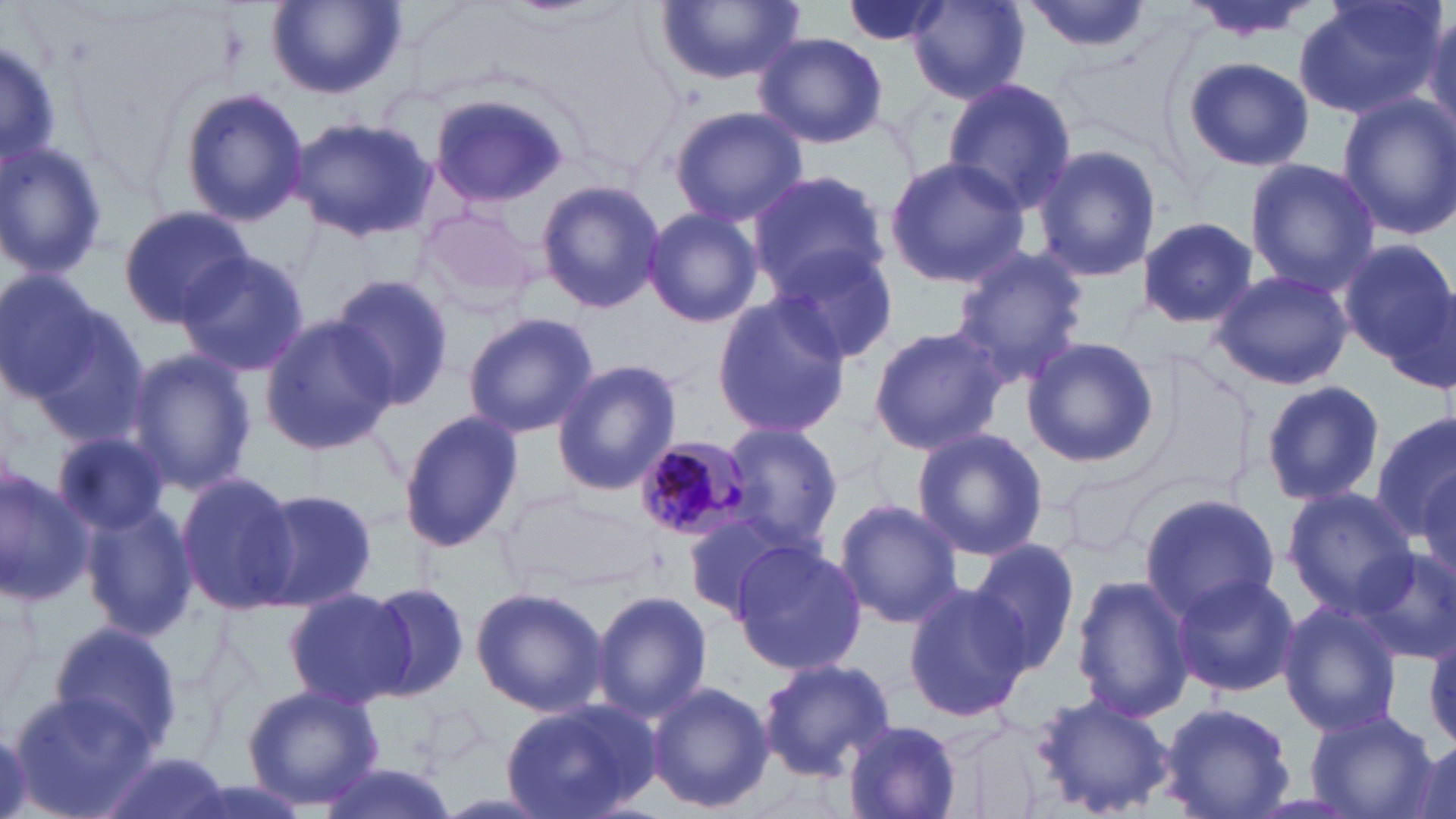
slide_level_diagnosis: Plasmodium malariae
image_size: 1456×819 pixels
magnification: 1000x
uninfected_red_blood_cell_locations: 'approximate bounding boxes as (x1, y1, x2, y2) in pixels: (266, 0, 405, 100), (837, 0, 953, 48), (1022, 0, 1154, 56), (1184, 0, 1319, 43), (1291, 0, 1446, 123), (656, 1, 804, 84), (909, 1, 1030, 103), (1421, 10, 1456, 140), (753, 32, 888, 149), (0, 36, 64, 175), (1180, 56, 1315, 172), (941, 78, 1077, 212), (179, 87, 308, 226), (426, 89, 573, 209), (1336, 93, 1456, 241), (667, 106, 808, 226), (288, 116, 436, 243), (0, 139, 108, 281), (1035, 143, 1162, 284), (883, 156, 1031, 285), (1241, 158, 1380, 292), (748, 169, 887, 295), (537, 178, 664, 314), (117, 205, 252, 329), (642, 206, 762, 328), (1134, 216, 1261, 327), (1338, 239, 1454, 366), (770, 245, 899, 365), (950, 246, 1089, 383), (176, 250, 310, 378), (0, 268, 111, 402), (1206, 268, 1357, 391), (329, 274, 454, 407), (8, 293, 146, 447), (710, 295, 852, 436), (462, 312, 598, 438), (258, 314, 397, 454), (866, 324, 1009, 457), (1018, 337, 1161, 468), (122, 347, 257, 497), (551, 359, 682, 496), (1259, 380, 1385, 505), (399, 408, 523, 553), (1372, 412, 1456, 539), (721, 424, 842, 550), (911, 427, 1048, 562), (52, 430, 172, 536), (1412, 463, 1456, 587), (0, 467, 92, 607), (1063, 469, 1158, 555), (175, 471, 299, 616), (1283, 485, 1421, 612), (249, 487, 377, 612), (1138, 491, 1281, 618), (835, 497, 961, 630), (81, 500, 194, 641), (682, 508, 810, 621), (971, 537, 1085, 673), (732, 540, 867, 677), (1352, 545, 1456, 664), (1170, 572, 1300, 698), (1072, 574, 1195, 724), (362, 580, 470, 703), (902, 582, 1033, 722), (470, 585, 607, 718), (283, 587, 412, 708), (589, 590, 712, 722), (1279, 601, 1403, 738), (48, 620, 185, 756), (757, 658, 896, 781), (646, 680, 775, 815), (242, 684, 384, 810), (7, 692, 153, 815), (1028, 693, 1174, 817), (500, 698, 665, 819), (1159, 702, 1294, 819), (1307, 711, 1436, 818), (841, 720, 964, 819), (100, 753, 232, 819), (311, 759, 458, 819)'
field_of_view: single
stain: May-Grünwald-Giemsa
modality: light microscopy
preparation: thin blood film
plasmodium_malariae_infected_red_blood_cell_locations: 'approximate bounding boxes as (x1, y1, x2, y2) in pixels: (631, 433, 757, 542)'